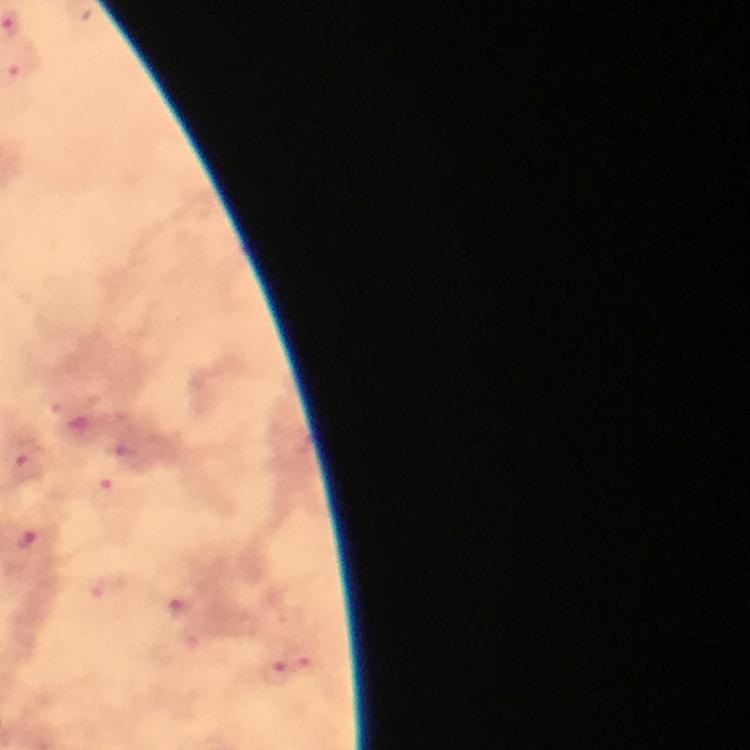
Approximate centers as (x, y) in pixels.
Summary:
  - Malaria parasite locations: (22, 71), (27, 457), (106, 494), (24, 540), (181, 608), (277, 675)
  - Preparation: thick smear
  - Immersion oil: applied
  - Context: from a malaria diagnostic workup
  - Stain: Giemsa
  - Capture: smartphone camera through the microscope
  - Image size: 750×750 pixels
  - Cropped from: one field of view
  - Magnification: 100x